Assess the morphology of the red blood cells.
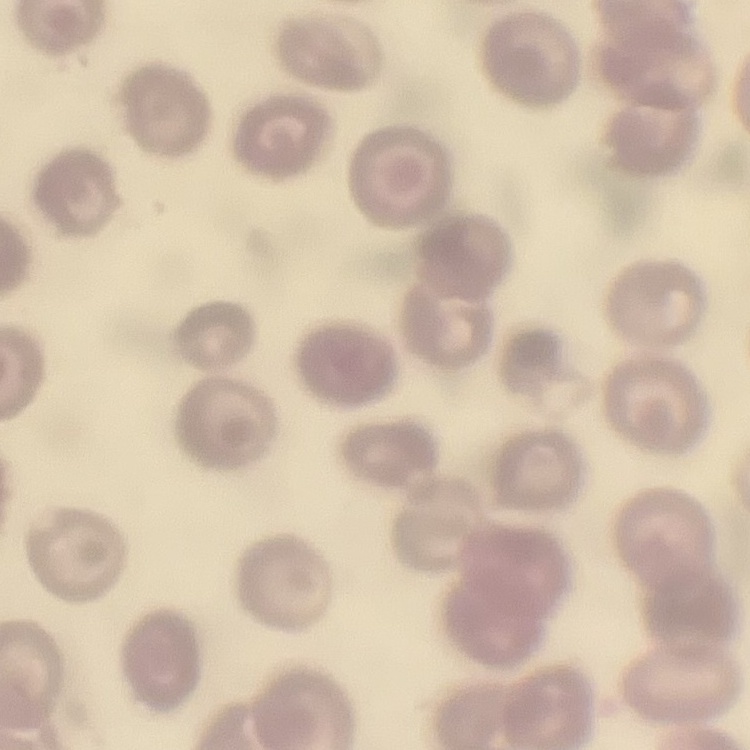

They show no rouleaux formation.

Summary:
  - Image type: square crop of a larger photomicrograph
  - Stain: Field's or Giemsa
  - Preparation: thin blood smear